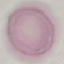 Result: negative for malaria parasites. Acquired by smartphone through the microscope eyepiece. Cell patch, automatically extracted from a larger field of view and resized to 64 × 64 pixels. Giemsa-stained preparation. Thin blood film.